Identify the cell.
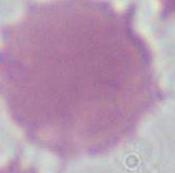
This is an erythrocyte.

Summary:
  - Modality: photomicrograph
  - Magnification: 1000x